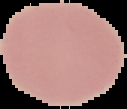
{
  "preparation": "thin blood film",
  "malaria_status": "uninfected",
  "image_type": "segmented cell region on a black background",
  "image_size": "127×109 pixels"
}